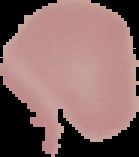
From a thin blood smear. Malaria status: uninfected. Image is 139×157 pixels. Segmented cell region on a black background.